Outline each blood parasite and name the species.
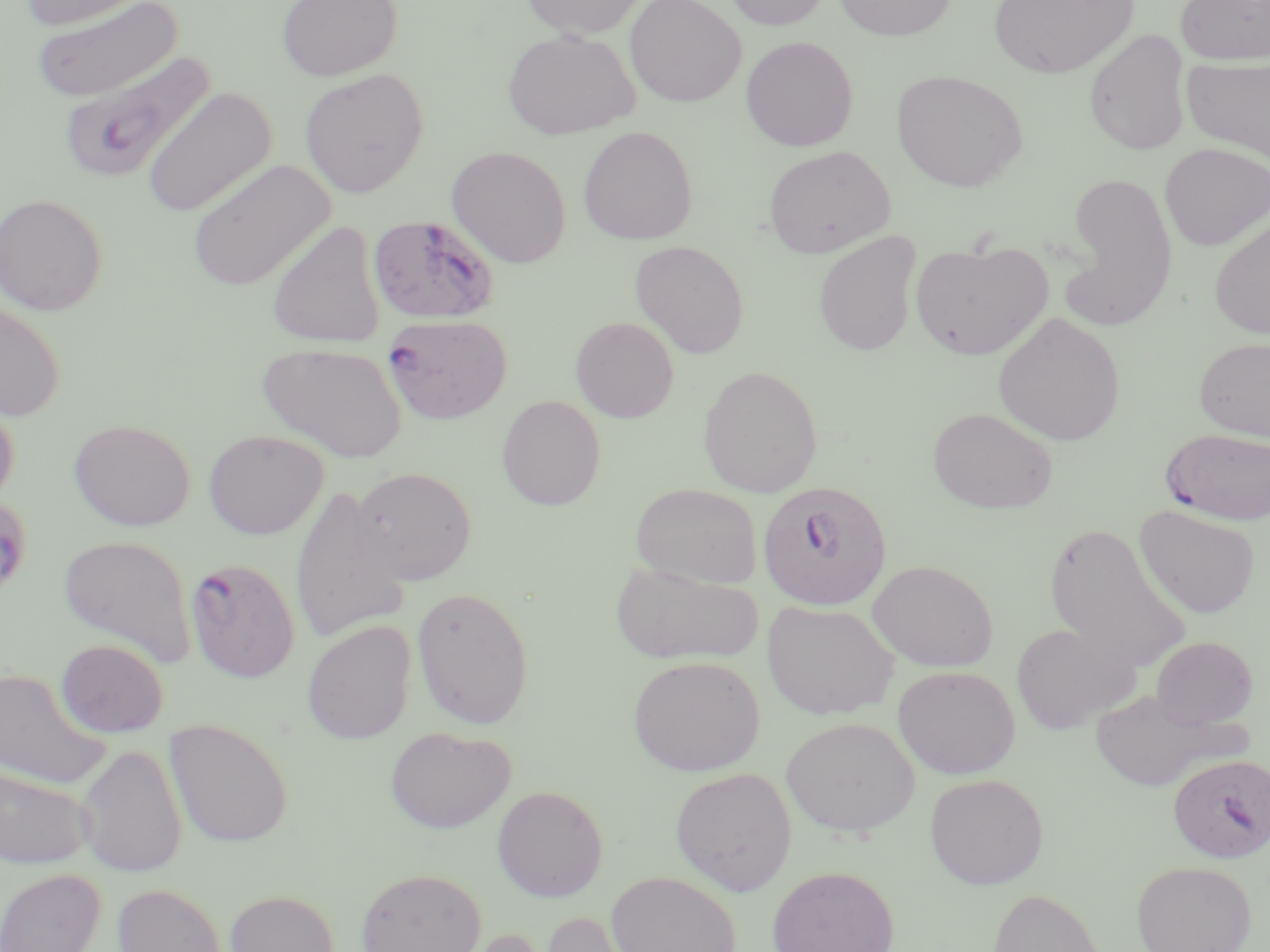
Approximate bounding boxes as (x1,y1)-(x2,y2) corner pairs in pixels.
Plasmodium falciparum-infected red blood cells: (58,51)-(215,185), (367,214)-(499,325), (382,313)-(512,424), (1161,427)-(1270,526), (757,480)-(892,611), (184,558)-(300,683), (1168,753)-(1269,863).
No Plasmodium ovale, Plasmodium malariae, Plasmodium vivax, Babesia divergens, or Trypanosoma brucei observed.

Summary:
  - Uninfected red blood cell locations: (18,0)-(154,30), (276,0)-(402,82), (519,0)-(647,38), (624,0)-(747,108), (722,0)-(833,31), (832,0)-(957,40), (988,0)-(1139,79), (1175,0)-(1270,65), (31,1)-(182,102), (502,28)-(639,140), (1084,29)-(1192,155), (740,36)-(858,152), (1182,55)-(1270,164), (299,68)-(429,198), (891,70)-(1029,192), (141,86)-(276,218), (577,126)-(698,246), (1160,143)-(1269,251), (763,145)-(895,258), (446,146)-(571,268), (185,158)-(336,292), (1059,173)-(1179,323), (0,193)-(108,316), (1209,215)-(1270,340), (266,220)-(387,349), (813,232)-(922,356), (630,240)-(749,359), (910,240)-(1052,360), (0,300)-(66,423), (992,311)-(1126,446), (570,316)-(679,423), (1194,337)-(1270,440), (258,341)-(408,463), (697,366)-(823,498), (0,393)-(20,509), (496,395)-(606,511), (927,407)-(1058,514), (68,418)-(196,531), (203,430)-(329,539), (349,466)-(477,586), (631,483)-(762,588), (288,484)-(411,645), (1134,505)-(1261,619), (1043,521)-(1191,672), (58,535)-(195,665), (610,560)-(764,666), (867,560)-(998,672), (411,586)-(534,730), (762,600)-(900,720), (302,621)-(417,744), (1010,623)-(1138,735), (1151,636)-(1257,729), (55,639)-(169,737), (627,655)-(764,776), (892,665)-(1021,779), (0,667)-(112,790), (1088,689)-(1235,792), (780,716)-(920,837), (164,718)-(293,847), (385,726)-(516,834), (76,744)-(187,877), (0,764)-(94,869), (670,767)-(797,896), (925,773)-(1049,889), (492,785)-(609,902), (1131,860)-(1257,952), (767,865)-(899,952), (355,866)-(487,952), (0,867)-(105,952), (606,871)-(741,952), (112,883)-(227,952), (988,887)-(1104,952), (225,889)-(339,952), (537,911)-(648,952), (449,926)-(553,952)
  - Slide-level diagnosis: Plasmodium falciparum
  - Magnification: 1000x
  - Image size: 1270×952 pixels
  - Modality: light microscopy
  - Field of view: one of a larger specimen
  - Preparation: thin blood film
  - Stain: May-Grünwald-Giemsa